Classify this cell by malaria status.
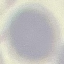
Uninfected.

Photographed with a smartphone camera at the microscope eyepiece. Automatically extracted cell patch, resized to 64 × 64 pixels. Giemsa-stained preparation. Thin blood film.